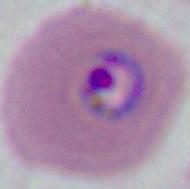
identification = Plasmodium
magnification = 400x or 1000x
modality = micrograph